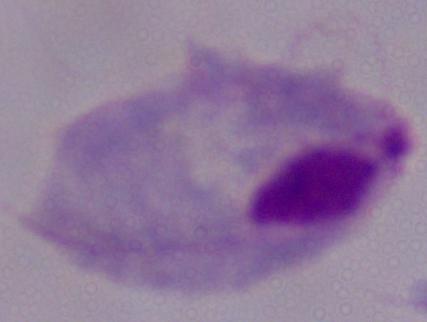
Micrograph. Captured at 1000x magnification. A trichomonad is seen.